Assess this cell for malaria.
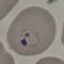
Parasitized.

Thin blood film. Giemsa stain. Automatically extracted cell patch, resized to 64 × 64 pixels. Photographed with a smartphone camera at the microscope eyepiece.